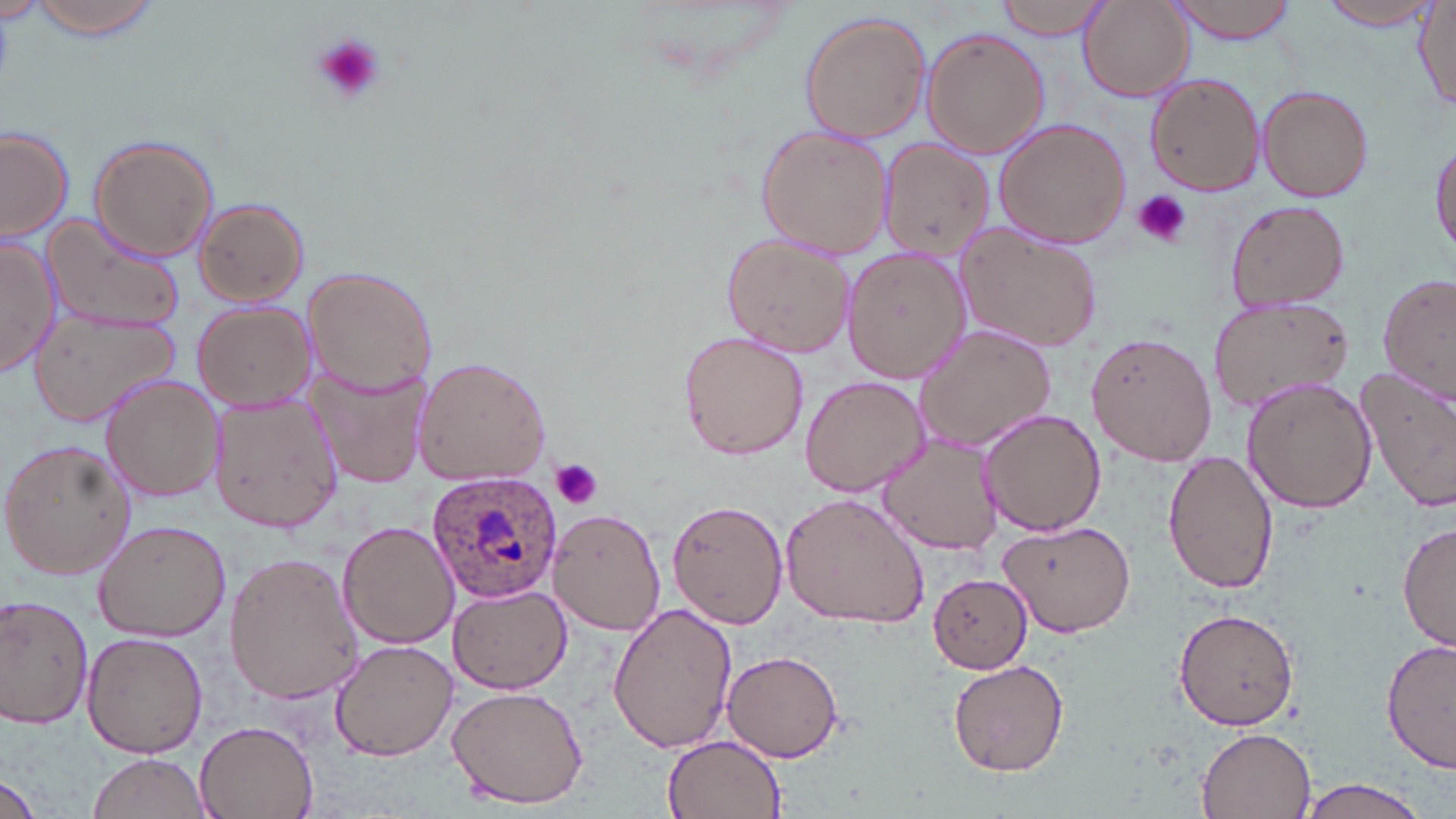

slide_level_diagnosis: Plasmodium ovale
image_size: 1456×819 pixels
field_of_view: single
stain: May-Grünwald-Giemsa
plasmodium_ovale_infected_red_blood_cell_locations: 'approximate bounding boxes as named x1/y1/x2/y2 corners in pixels: (x1=431, y1=467, x2=562, y2=606)'
modality: optical microscopy
platelet_locations: 'approximate bounding boxes as named x1/y1/x2/y2 corners in pixels: (x1=309, y1=33, x2=387, y2=107), (x1=1133, y1=189, x2=1191, y2=249), (x1=550, y1=460, x2=603, y2=510)'
uninfected_red_blood_cell_locations: 'approximate bounding boxes as named x1/y1/x2/y2 corners in pixels: (x1=24, y1=0, x2=165, y2=39), (x1=1163, y1=0, x2=1303, y2=42), (x1=1077, y1=1, x2=1191, y2=102), (x1=1314, y1=1, x2=1440, y2=29), (x1=992, y1=2, x2=1113, y2=39), (x1=1414, y1=4, x2=1455, y2=113), (x1=800, y1=14, x2=930, y2=143), (x1=922, y1=28, x2=1050, y2=159), (x1=1145, y1=73, x2=1265, y2=194), (x1=1257, y1=85, x2=1375, y2=202), (x1=992, y1=115, x2=1134, y2=250), (x1=0, y1=125, x2=75, y2=244), (x1=756, y1=125, x2=892, y2=259), (x1=1430, y1=133, x2=1456, y2=264), (x1=90, y1=134, x2=219, y2=262), (x1=878, y1=139, x2=993, y2=260), (x1=194, y1=198, x2=308, y2=307), (x1=1224, y1=198, x2=1351, y2=311), (x1=44, y1=213, x2=190, y2=334), (x1=955, y1=223, x2=1101, y2=352), (x1=722, y1=233, x2=855, y2=359), (x1=0, y1=237, x2=59, y2=378), (x1=843, y1=246, x2=969, y2=384), (x1=304, y1=266, x2=437, y2=397), (x1=1377, y1=270, x2=1454, y2=405), (x1=1208, y1=297, x2=1354, y2=413), (x1=193, y1=303, x2=312, y2=411), (x1=29, y1=307, x2=180, y2=426), (x1=914, y1=326, x2=1055, y2=450), (x1=1086, y1=329, x2=1217, y2=467), (x1=679, y1=331, x2=808, y2=462), (x1=412, y1=357, x2=551, y2=486), (x1=304, y1=363, x2=430, y2=491), (x1=1356, y1=364, x2=1456, y2=510), (x1=101, y1=373, x2=224, y2=502), (x1=801, y1=375, x2=927, y2=496), (x1=1239, y1=378, x2=1376, y2=511), (x1=209, y1=393, x2=341, y2=532), (x1=978, y1=408, x2=1106, y2=537), (x1=881, y1=434, x2=1000, y2=555), (x1=0, y1=440, x2=135, y2=580), (x1=1163, y1=451, x2=1281, y2=594), (x1=778, y1=492, x2=930, y2=629), (x1=667, y1=499, x2=788, y2=628), (x1=550, y1=506, x2=668, y2=634), (x1=93, y1=518, x2=230, y2=641), (x1=997, y1=519, x2=1137, y2=638), (x1=338, y1=520, x2=459, y2=649), (x1=1399, y1=521, x2=1456, y2=655), (x1=224, y1=551, x2=363, y2=705), (x1=927, y1=573, x2=1032, y2=673), (x1=449, y1=585, x2=570, y2=695), (x1=0, y1=595, x2=95, y2=729), (x1=609, y1=602, x2=737, y2=754), (x1=1174, y1=607, x2=1301, y2=731), (x1=81, y1=632, x2=208, y2=759), (x1=1381, y1=635, x2=1456, y2=775), (x1=329, y1=639, x2=457, y2=761), (x1=723, y1=649, x2=845, y2=763), (x1=949, y1=659, x2=1069, y2=776), (x1=447, y1=682, x2=588, y2=809), (x1=193, y1=722, x2=317, y2=818), (x1=1195, y1=726, x2=1317, y2=818), (x1=663, y1=734, x2=786, y2=819), (x1=87, y1=754, x2=212, y2=819), (x1=1292, y1=776, x2=1437, y2=819), (x1=0, y1=777, x2=47, y2=819)'
preparation: thin blood smear
magnification: 1000x